Assess this cell for malaria.
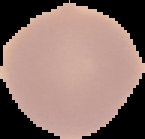

It is uninfected.

preparation: thin blood film
image_type: segmented cell region on a black background
image_size: 145×139 pixels